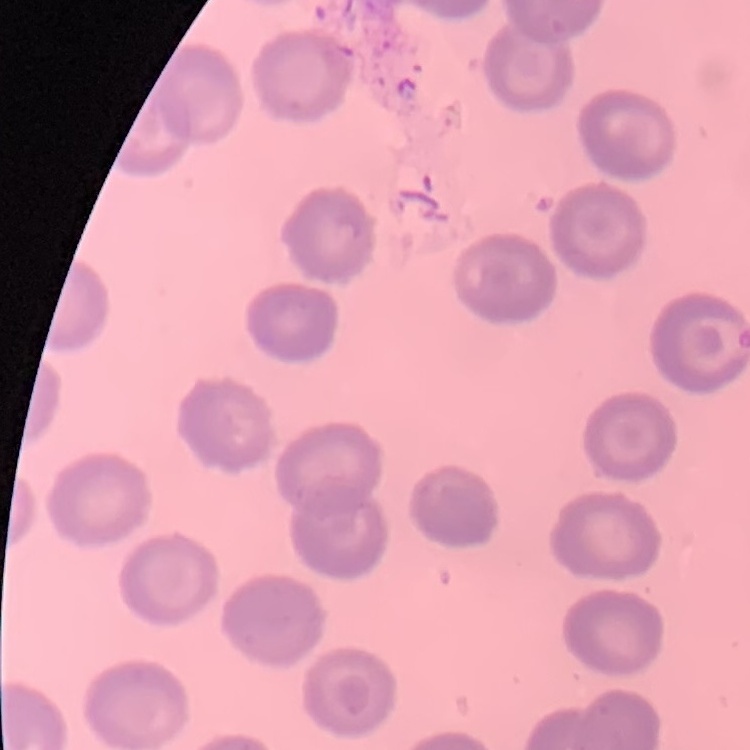

The red blood cells exhibit no rouleaux formation. Stained with either Field's or Giemsa. One tile cut from a larger photomicrograph. Thin blood smear.